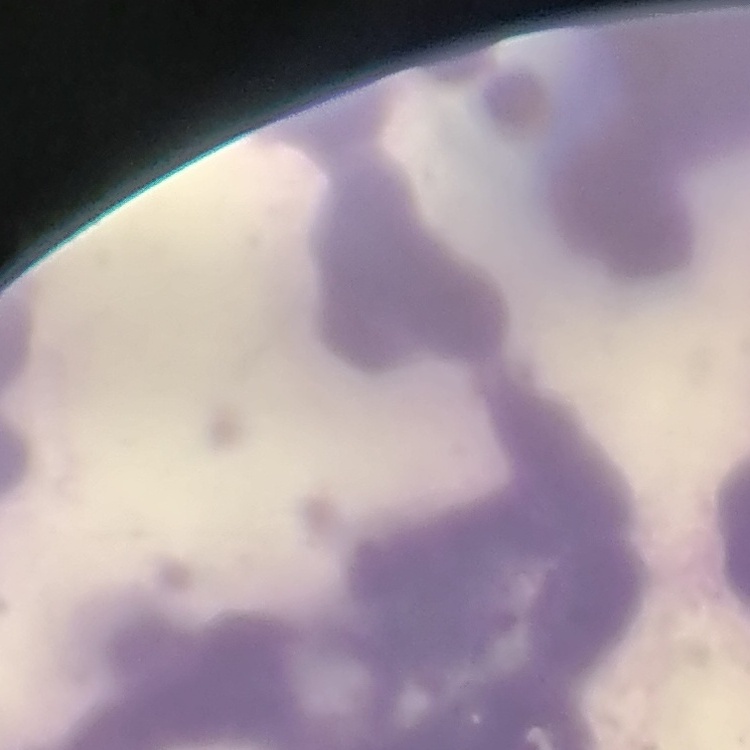
red_blood_cell_morphology: rouleaux formation
preparation: thin blood smear
image_type: one tile cut from a larger photomicrograph
stain: Field's or Giemsa